Report the malaria status of this cell.
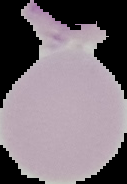
It is uninfected.

Summary:
  - Image size: 127×184 pixels
  - Preparation: thin blood smear
  - Image type: segmented cell region on a black background